Classify this cell by malaria status.
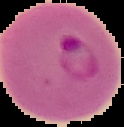

Parasitized.

preparation = thin blood film
image type = segmented cell region on a black background
image size = 124×127 pixels